Identify the blood parasite species.
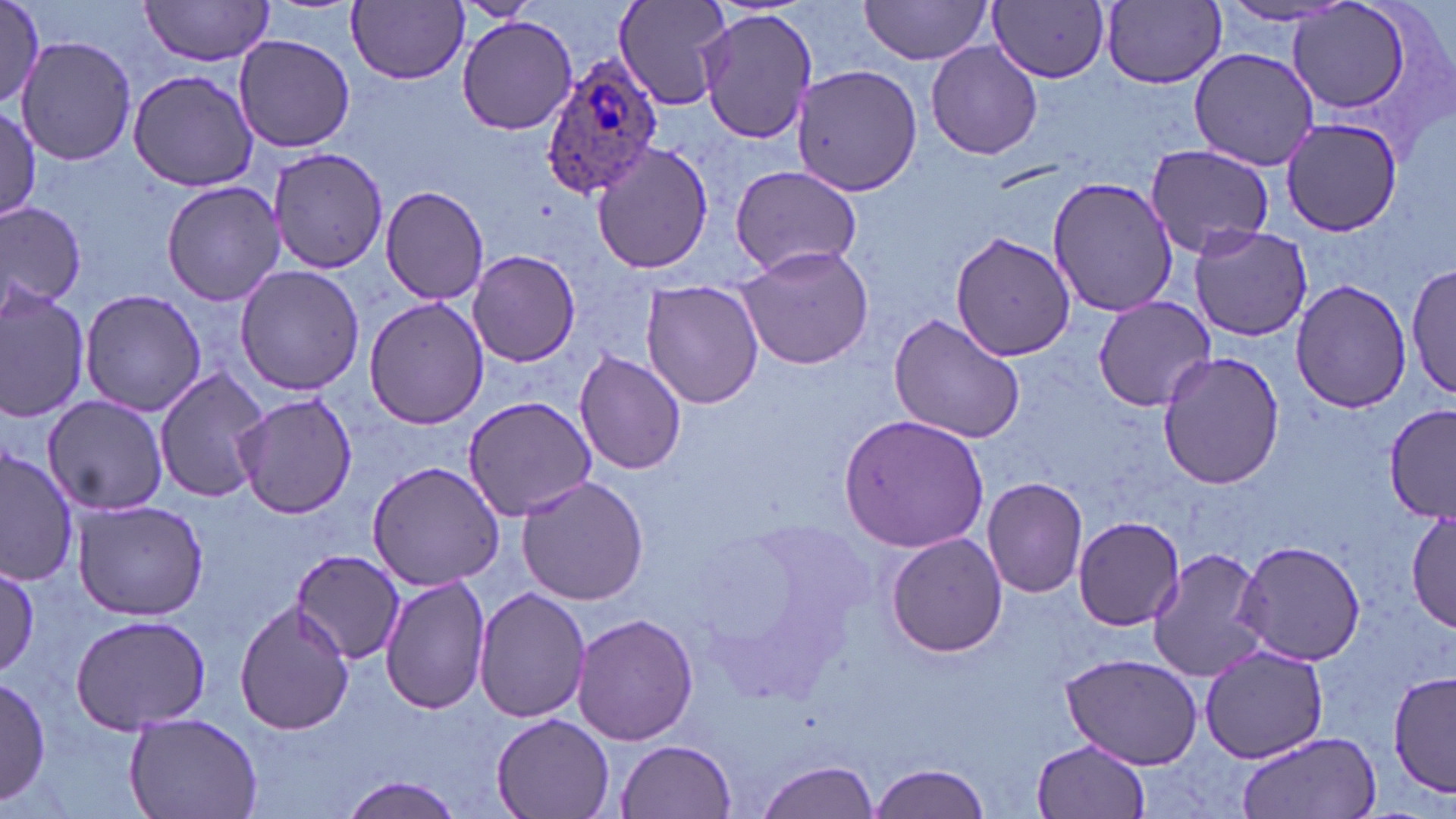
Plasmodium ovale.

Approximate bounding boxes as [x1, y1, x2, y2] in pixels. Plasmodium ovale-infected red blood cell locations: [541, 52, 664, 201]. Uninfected red blood cell locations: [0, 0, 50, 117], [138, 0, 276, 66], [453, 0, 542, 24], [613, 0, 735, 111], [348, 1, 469, 85], [858, 1, 995, 64], [989, 1, 1111, 82], [1099, 1, 1228, 87], [1211, 1, 1361, 29], [1286, 1, 1418, 115], [695, 9, 817, 143], [457, 17, 578, 135], [233, 33, 355, 153], [16, 36, 137, 167], [925, 41, 1042, 161], [1190, 47, 1320, 171], [790, 63, 924, 197], [127, 69, 261, 191], [0, 106, 42, 224], [1281, 117, 1403, 236], [591, 141, 714, 273], [1143, 145, 1276, 258], [271, 148, 389, 274], [728, 163, 862, 278], [1048, 175, 1176, 319], [161, 179, 288, 307], [380, 186, 490, 306], [0, 203, 86, 306], [1189, 224, 1313, 342], [949, 231, 1076, 361], [736, 243, 877, 372], [467, 250, 581, 367], [1408, 263, 1456, 404], [234, 264, 366, 395], [1290, 279, 1414, 413], [641, 280, 765, 409], [0, 285, 91, 424], [78, 287, 207, 416], [1092, 295, 1215, 412], [364, 296, 488, 430], [887, 313, 1026, 444], [574, 351, 688, 476], [1158, 351, 1285, 490], [152, 367, 269, 503], [233, 391, 360, 519], [43, 394, 169, 517], [462, 395, 601, 521], [1383, 404, 1456, 521], [839, 413, 991, 553], [0, 447, 77, 585], [366, 460, 507, 590], [515, 475, 651, 607], [983, 478, 1088, 598], [70, 497, 210, 622], [1407, 503, 1454, 633], [1073, 515, 1184, 630], [886, 532, 1009, 659], [1236, 540, 1366, 665], [1147, 547, 1271, 684], [291, 549, 405, 665], [0, 567, 41, 677], [380, 572, 492, 716], [474, 587, 590, 724], [234, 600, 356, 736], [67, 611, 214, 736], [571, 612, 699, 745], [1199, 644, 1329, 763], [1059, 649, 1206, 772], [1389, 670, 1454, 797], [0, 674, 51, 810], [124, 712, 263, 819], [491, 713, 614, 819], [1235, 731, 1382, 819], [1032, 737, 1152, 819], [616, 740, 736, 818], [753, 760, 879, 819], [868, 762, 991, 819], [338, 776, 465, 818]. Image is 1456×819 pixels. Light microscopy. One field of a larger specimen. May-Grünwald-Giemsa-stained preparation. Thin blood film. Captured at 1000x magnification.